State which parasite is depicted.
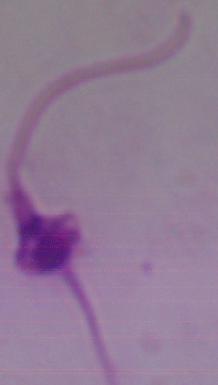

Leishmania.

Summary:
  - Modality: micrograph
  - Magnification: 1000x